Identify the parasite.
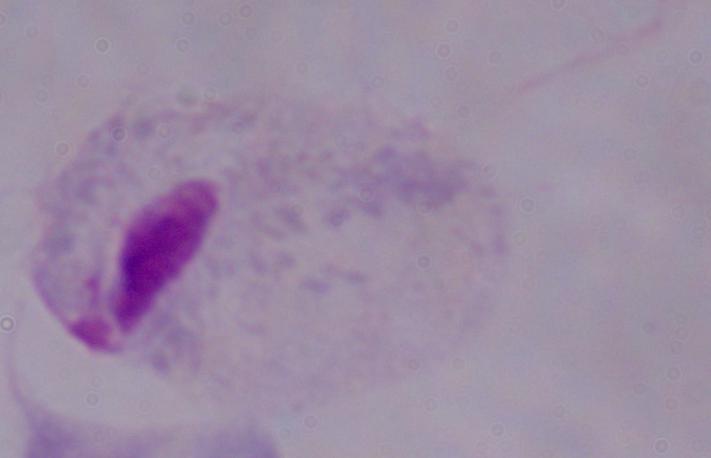
A trichomonad.

1000x magnification. Micrograph.